Identify the parasite.
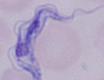
This is a trypanosome.

{
  "magnification": "1000x",
  "modality": "micrograph"
}